Report the malaria status of this cell.
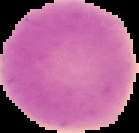
Uninfected.

Summary:
  - Preparation: thin blood smear
  - Image size: 139×133 pixels
  - Image type: segmented cell region on a black background